State which parasite is depicted.
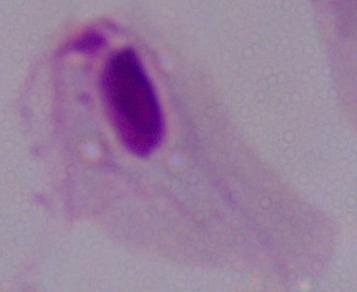

This is a trichomonad.

magnification = 1000x
modality = micrograph